Locate every cell, classifying each as a parasitized red blood cell, an uninfected red blood cell, or a white blood cell.
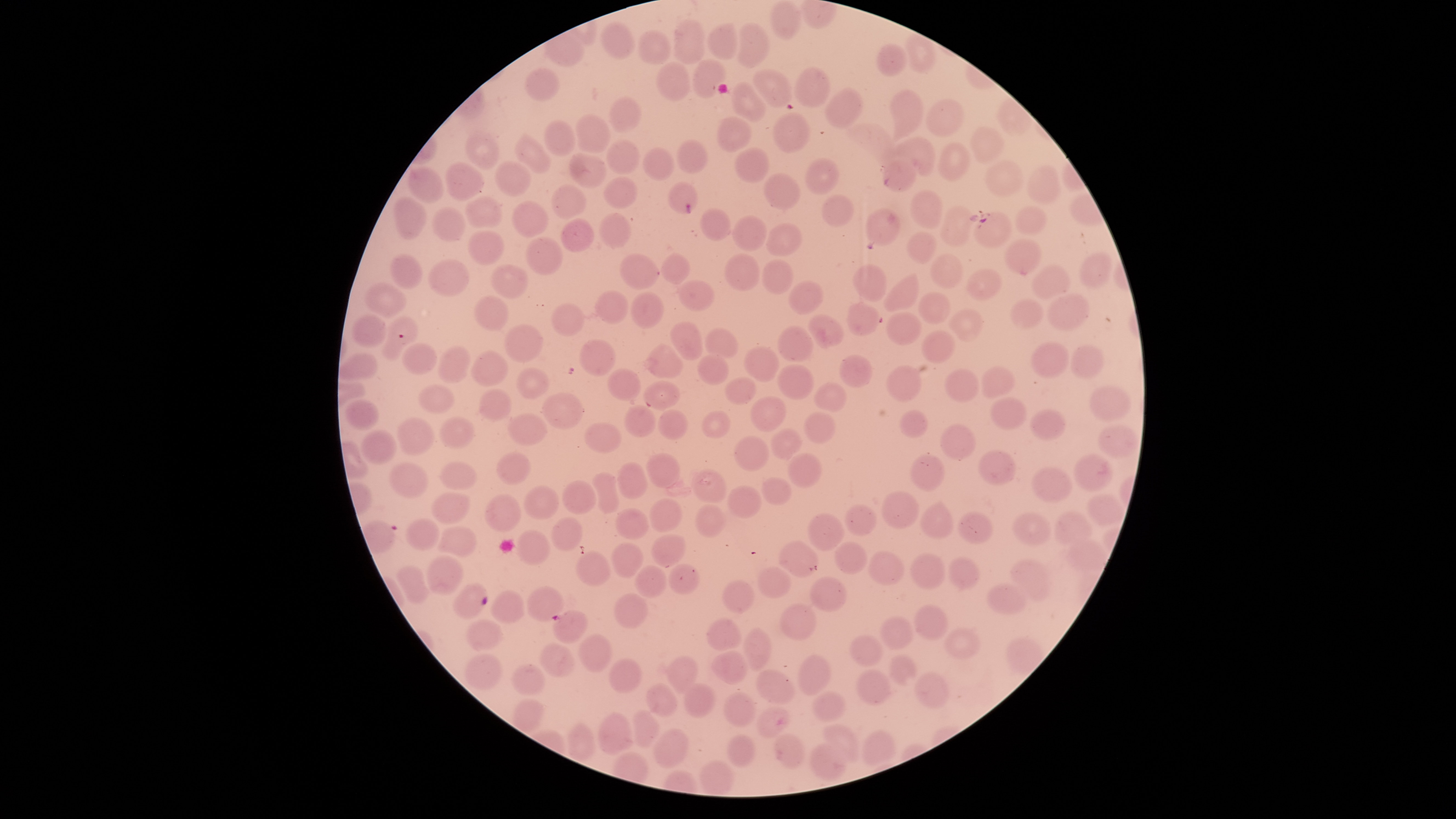
Approximate bounding boxes, in pixels from the top-left corner.
Parasitized red blood cells: (left=667, top=181, right=697, bottom=215), (left=971, top=211, right=1012, bottom=249), (left=379, top=316, right=419, bottom=361), (left=453, top=583, right=488, bottom=617), (left=552, top=609, right=588, bottom=644).
Uninfected red blood cells: (left=770, top=1, right=802, bottom=40), (left=674, top=20, right=704, bottom=65), (left=600, top=23, right=637, bottom=60), (left=706, top=23, right=739, bottom=59), (left=737, top=23, right=769, bottom=69), (left=638, top=29, right=673, bottom=65), (left=876, top=43, right=909, bottom=76), (left=691, top=57, right=726, bottom=99), (left=655, top=61, right=692, bottom=102), (left=524, top=68, right=559, bottom=101), (left=795, top=68, right=828, bottom=107), (left=753, top=69, right=792, bottom=106), (left=731, top=81, right=766, bottom=123), (left=825, top=88, right=862, bottom=127), (left=890, top=90, right=923, bottom=142), (left=609, top=97, right=642, bottom=134), (left=925, top=99, right=963, bottom=137), (left=773, top=112, right=811, bottom=153), (left=575, top=116, right=610, bottom=153), (left=716, top=117, right=751, bottom=151), (left=544, top=120, right=576, bottom=156), (left=847, top=123, right=895, bottom=167), (left=970, top=126, right=1005, bottom=162), (left=465, top=133, right=499, bottom=169), (left=515, top=134, right=551, bottom=174), (left=889, top=138, right=936, bottom=177), (left=607, top=139, right=639, bottom=176), (left=677, top=140, right=708, bottom=173), (left=937, top=144, right=970, bottom=181), (left=642, top=147, right=674, bottom=182), (left=733, top=147, right=769, bottom=185), (left=568, top=153, right=608, bottom=187), (left=805, top=157, right=839, bottom=196), (left=494, top=159, right=532, bottom=196), (left=882, top=160, right=918, bottom=194), (left=986, top=161, right=1023, bottom=197), (left=445, top=162, right=485, bottom=202), (left=1027, top=165, right=1062, bottom=205), (left=409, top=167, right=443, bottom=202), (left=763, top=172, right=801, bottom=210), (left=602, top=177, right=640, bottom=208), (left=551, top=184, right=586, bottom=219), (left=910, top=189, right=943, bottom=230), (left=820, top=194, right=856, bottom=227), (left=465, top=197, right=503, bottom=229), (left=393, top=198, right=427, bottom=242), (left=511, top=200, right=548, bottom=237), (left=936, top=204, right=978, bottom=246), (left=432, top=205, right=465, bottom=242), (left=1015, top=205, right=1046, bottom=236), (left=699, top=208, right=731, bottom=242), (left=865, top=208, right=901, bottom=246), (left=597, top=214, right=633, bottom=249), (left=732, top=215, right=767, bottom=251), (left=562, top=218, right=594, bottom=252), (left=767, top=223, right=801, bottom=256), (left=467, top=231, right=504, bottom=265), (left=907, top=232, right=938, bottom=265), (left=526, top=236, right=563, bottom=275), (left=1004, top=240, right=1043, bottom=275), (left=660, top=252, right=690, bottom=285), (left=390, top=253, right=423, bottom=290), (left=930, top=253, right=963, bottom=287), (left=620, top=254, right=659, bottom=289), (left=724, top=254, right=761, bottom=292), (left=1080, top=254, right=1112, bottom=287), (left=428, top=259, right=468, bottom=298), (left=761, top=259, right=794, bottom=295), (left=491, top=263, right=529, bottom=298), (left=852, top=264, right=887, bottom=302), (left=1030, top=265, right=1071, bottom=302), (left=966, top=269, right=1002, bottom=301), (left=883, top=272, right=920, bottom=312), (left=677, top=279, right=713, bottom=311), (left=787, top=280, right=823, bottom=314), (left=365, top=283, right=406, bottom=316), (left=594, top=289, right=630, bottom=326), (left=918, top=291, right=953, bottom=323), (left=631, top=292, right=663, bottom=329), (left=1047, top=292, right=1089, bottom=331), (left=475, top=295, right=508, bottom=331), (left=1011, top=298, right=1046, bottom=327), (left=846, top=303, right=881, bottom=335), (left=551, top=304, right=584, bottom=337), (left=947, top=309, right=984, bottom=341), (left=887, top=313, right=921, bottom=346), (left=353, top=315, right=385, bottom=347), (left=808, top=315, right=843, bottom=349), (left=670, top=322, right=702, bottom=360), (left=504, top=323, right=543, bottom=363), (left=778, top=325, right=815, bottom=361), (left=705, top=329, right=737, bottom=357), (left=922, top=330, right=955, bottom=363), (left=578, top=339, right=616, bottom=375), (left=645, top=343, right=684, bottom=380), (left=1030, top=343, right=1071, bottom=379), (left=401, top=344, right=436, bottom=375), (left=1071, top=344, right=1105, bottom=378), (left=438, top=347, right=471, bottom=384), (left=744, top=347, right=780, bottom=382), (left=471, top=350, right=508, bottom=387), (left=339, top=352, right=378, bottom=380), (left=840, top=354, right=874, bottom=388), (left=697, top=355, right=729, bottom=386), (left=777, top=364, right=814, bottom=400), (left=886, top=365, right=923, bottom=401), (left=981, top=366, right=1016, bottom=400), (left=515, top=368, right=550, bottom=398), (left=944, top=368, right=979, bottom=404), (left=607, top=370, right=642, bottom=400), (left=725, top=378, right=757, bottom=405), (left=644, top=379, right=680, bottom=409), (left=813, top=382, right=845, bottom=412), (left=417, top=385, right=456, bottom=415), (left=1087, top=385, right=1131, bottom=423), (left=479, top=388, right=513, bottom=421), (left=542, top=392, right=581, bottom=428), (left=748, top=395, right=786, bottom=433), (left=989, top=397, right=1027, bottom=430), (left=345, top=399, right=380, bottom=430), (left=624, top=405, right=656, bottom=437), (left=657, top=409, right=687, bottom=441), (left=899, top=409, right=928, bottom=439), (left=1030, top=409, right=1067, bottom=439), (left=702, top=410, right=730, bottom=438), (left=804, top=412, right=836, bottom=443), (left=508, top=415, right=548, bottom=445), (left=397, top=417, right=436, bottom=456), (left=438, top=418, right=476, bottom=449), (left=584, top=423, right=622, bottom=452), (left=940, top=424, right=976, bottom=460), (left=772, top=426, right=803, bottom=460), (left=1099, top=426, right=1139, bottom=457), (left=361, top=432, right=398, bottom=465), (left=734, top=435, right=769, bottom=472), (left=978, top=450, right=1016, bottom=485), (left=1073, top=452, right=1114, bottom=492), (left=496, top=453, right=531, bottom=484), (left=646, top=453, right=681, bottom=488), (left=786, top=453, right=822, bottom=488), (left=909, top=453, right=945, bottom=490), (left=617, top=461, right=648, bottom=499), (left=389, top=463, right=428, bottom=499), (left=440, top=463, right=477, bottom=491), (left=1032, top=467, right=1073, bottom=501), (left=692, top=468, right=726, bottom=502), (left=590, top=472, right=619, bottom=513), (left=761, top=476, right=793, bottom=506), (left=562, top=480, right=597, bottom=515), (left=523, top=485, right=559, bottom=519), (left=727, top=486, right=763, bottom=517), (left=881, top=491, right=918, bottom=528), (left=430, top=492, right=472, bottom=525), (left=484, top=493, right=522, bottom=532), (left=1087, top=494, right=1125, bottom=523), (left=650, top=497, right=682, bottom=531), (left=921, top=502, right=955, bottom=541), (left=845, top=503, right=875, bottom=536), (left=695, top=504, right=725, bottom=537), (left=615, top=507, right=650, bottom=540), (left=1055, top=511, right=1093, bottom=544), (left=807, top=512, right=843, bottom=551), (left=957, top=512, right=992, bottom=545), (left=1014, top=513, right=1048, bottom=544), (left=550, top=518, right=584, bottom=549), (left=407, top=519, right=442, bottom=550), (left=439, top=526, right=475, bottom=556), (left=516, top=530, right=549, bottom=565), (left=651, top=534, right=686, bottom=567), (left=1066, top=540, right=1109, bottom=571), (left=780, top=541, right=817, bottom=578), (left=834, top=541, right=866, bottom=573), (left=611, top=542, right=643, bottom=578), (left=868, top=550, right=905, bottom=585), (left=576, top=551, right=611, bottom=586), (left=908, top=553, right=945, bottom=591), (left=425, top=556, right=465, bottom=595), (left=948, top=557, right=980, bottom=591), (left=1011, top=558, right=1050, bottom=603), (left=668, top=564, right=700, bottom=594), (left=396, top=565, right=428, bottom=604), (left=634, top=565, right=667, bottom=596), (left=756, top=567, right=791, bottom=597), (left=809, top=577, right=847, bottom=613), (left=722, top=581, right=754, bottom=614), (left=987, top=582, right=1028, bottom=614), (left=526, top=586, right=564, bottom=622), (left=490, top=591, right=524, bottom=625), (left=614, top=593, right=648, bottom=627), (left=779, top=602, right=819, bottom=642), (left=914, top=604, right=948, bottom=642), (left=880, top=614, right=914, bottom=650), (left=706, top=618, right=743, bottom=651), (left=466, top=620, right=501, bottom=650), (left=742, top=628, right=772, bottom=670), (left=944, top=628, right=979, bottom=658), (left=578, top=633, right=613, bottom=673), (left=850, top=635, right=884, bottom=667), (left=539, top=643, right=577, bottom=679), (left=711, top=650, right=747, bottom=685), (left=464, top=653, right=502, bottom=689), (left=797, top=653, right=832, bottom=695), (left=889, top=654, right=919, bottom=685), (left=667, top=656, right=697, bottom=695), (left=609, top=657, right=642, bottom=693), (left=510, top=664, right=547, bottom=694), (left=754, top=669, right=796, bottom=705), (left=855, top=669, right=893, bottom=708), (left=915, top=673, right=950, bottom=708), (left=682, top=682, right=716, bottom=720), (left=647, top=684, right=678, bottom=715), (left=814, top=690, right=846, bottom=722), (left=723, top=692, right=756, bottom=727), (left=754, top=707, right=789, bottom=737), (left=633, top=709, right=660, bottom=747), (left=599, top=712, right=635, bottom=755), (left=823, top=725, right=860, bottom=762), (left=654, top=728, right=690, bottom=769), (left=862, top=729, right=896, bottom=764), (left=726, top=733, right=756, bottom=769), (left=774, top=735, right=804, bottom=768), (left=810, top=742, right=850, bottom=780), (left=699, top=761, right=734, bottom=795).
No white blood cells identified.

Single field of view. The visible region is circular. Smartphone photograph through the microscope eyepiece. Image is 1456×819 pixels. Giemsa-stained preparation. Species: Plasmodium falciparum. Thin blood smear.